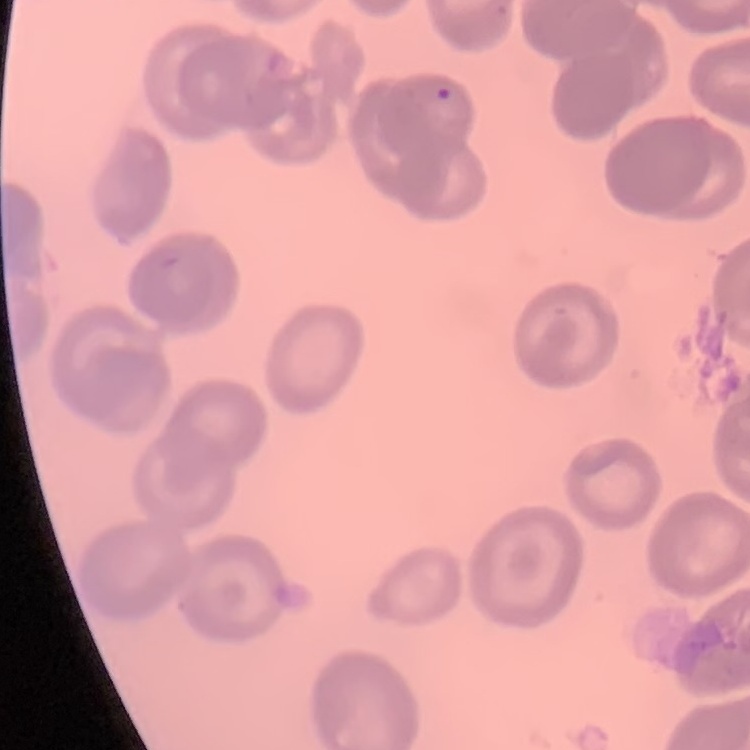
The erythrocytes exhibit no rouleaux formation. One tile cut from a larger photomicrograph. Field's or Giemsa stain. Thin blood smear.